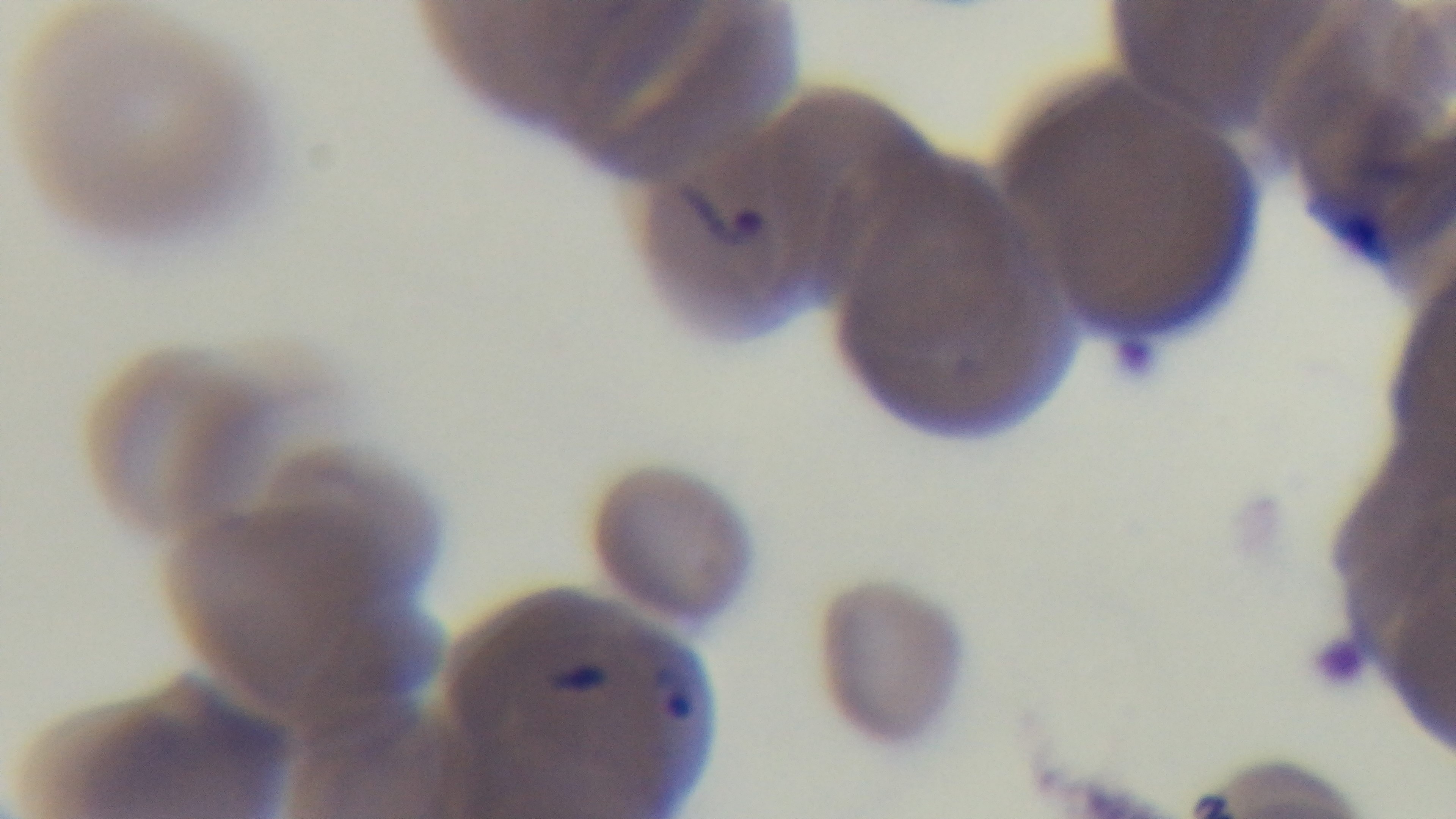
Summary:
  - Capture: mounted 4K digital camera
  - Preparation: thin
  - Objective: 100x oil immersion
  - Field of view: single
  - Stain: Giemsa
  - Malaria status: positive
  - Modality: light microscopy